Assess the morphology of the erythrocytes.
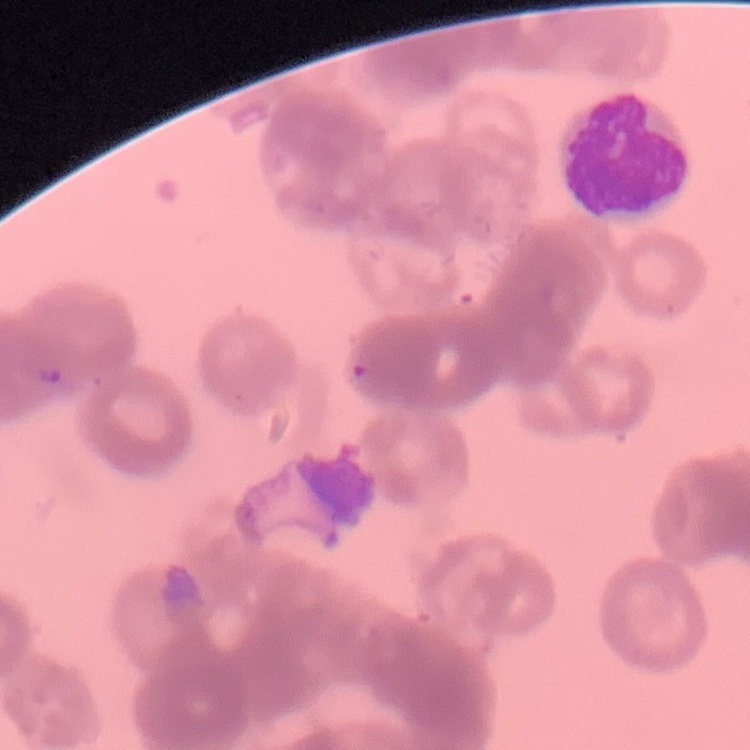
Rouleaux formation.

preparation = thin blood smear
image type = one tile cut from a larger photomicrograph
stain = Field's or Giemsa